Locate every malaria parasite.
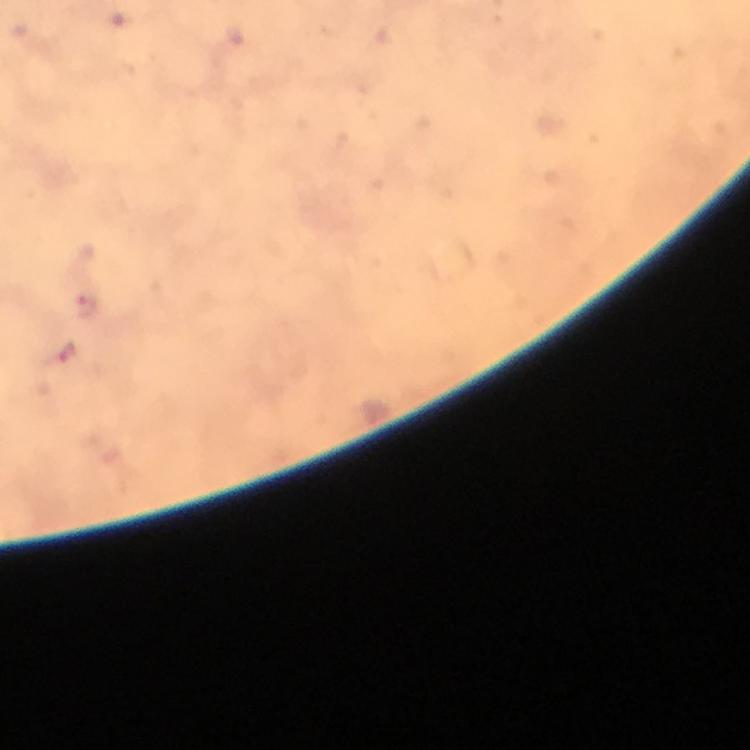

Approximate centers as {x, y} in pixels.
Malaria parasites: {88, 308}, {66, 354}.

Summary:
  - Context: from a malaria diagnostic workup
  - Cropped from: one field of view
  - Immersion oil: applied
  - Stain: Giemsa
  - Capture: smartphone camera through the microscope
  - Preparation: thick blood smear
  - Magnification: 100x
  - Image size: 750×750 pixels